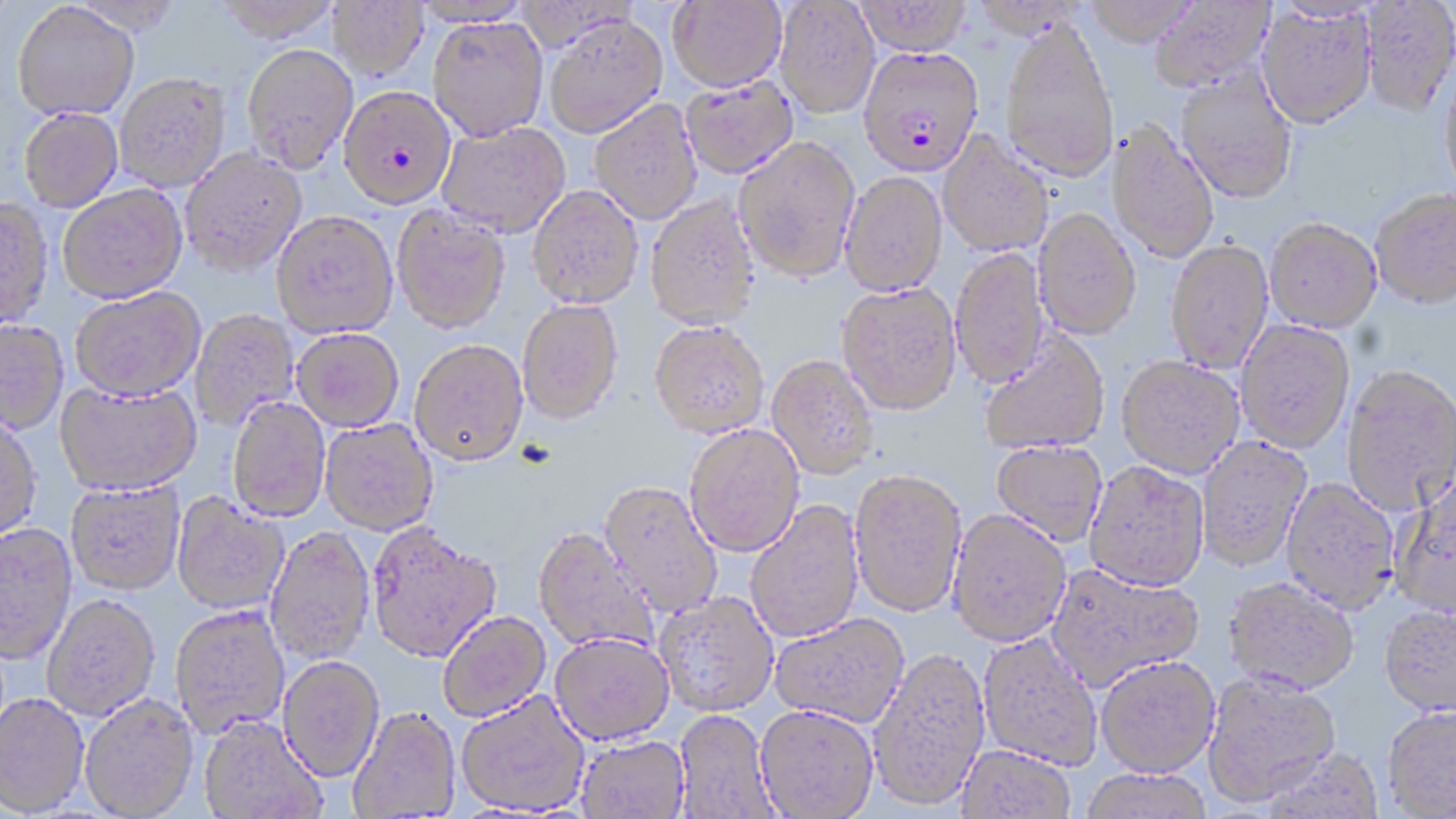

Summary:
  - Coordinate format: approximate bounding boxes as (x1,y1)-(x2,y2) corner pairs in pixels
  - Uninfected red blood cell locations: (213,0)-(343,42), (854,0)-(973,56), (1083,0)-(1201,47), (1149,0)-(1276,94), (326,1)-(429,81), (667,1)-(787,92), (775,1)-(880,119), (1360,1)-(1456,120), (12,3)-(139,123), (1257,6)-(1377,130), (543,14)-(668,139), (427,16)-(549,142), (1001,17)-(1119,183), (241,43)-(359,174), (1439,68)-(1456,202), (1174,70)-(1299,206), (115,73)-(231,192), (680,78)-(797,179), (590,99)-(702,225), (19,110)-(123,213), (438,121)-(570,239), (1105,123)-(1220,265), (937,131)-(1053,258), (734,136)-(860,283), (180,147)-(308,277), (840,172)-(948,297), (527,185)-(644,309), (58,186)-(187,305), (1370,191)-(1456,312), (645,195)-(761,330), (0,200)-(54,332), (392,205)-(511,335), (1033,209)-(1141,342), (272,212)-(398,339), (1265,221)-(1382,336), (1165,242)-(1273,375), (951,248)-(1049,390), (837,284)-(962,418), (71,288)-(205,404), (518,299)-(624,426), (191,310)-(299,431), (1236,321)-(1355,455), (0,322)-(68,435), (649,322)-(769,439), (291,329)-(404,432), (980,331)-(1110,456), (410,342)-(529,469), (767,356)-(879,480), (1116,358)-(1244,481), (1341,367)-(1456,516), (55,383)-(202,498), (227,398)-(331,523), (0,419)-(43,545), (320,420)-(437,536), (685,425)-(805,558), (1196,437)-(1311,573), (991,442)-(1107,547), (1085,463)-(1210,595), (849,473)-(966,620), (1390,477)-(1456,623), (1281,478)-(1400,617), (65,481)-(186,597), (599,483)-(723,619), (171,493)-(290,616), (746,500)-(864,644), (947,512)-(1072,650), (0,524)-(78,668), (366,524)-(501,666), (266,528)-(375,666), (533,528)-(658,655), (1045,565)-(1205,694), (1223,580)-(1358,698), (654,592)-(779,718), (42,597)-(161,722), (170,606)-(290,739), (1379,608)-(1456,719), (439,612)-(552,724), (770,616)-(910,731), (977,633)-(1103,772), (550,636)-(675,747), (869,649)-(990,814), (278,658)-(384,785), (1096,659)-(1221,781), (1202,674)-(1341,809), (456,692)-(590,817), (0,694)-(89,818), (80,695)-(200,819), (754,707)-(879,819), (1381,707)-(1456,818), (348,709)-(461,817), (673,710)-(778,819), (199,717)-(327,819), (576,737)-(690,819), (956,746)-(1077,818), (1256,749)-(1386,819), (1079,770)-(1213,819)
  - Plasmodium falciparum-infected red blood cell locations: (858,46)-(984,179), (338,85)-(457,211)
  - Slide-level diagnosis: Plasmodium falciparum
  - Stain: May-Grünwald-Giemsa
  - Magnification: 1000x
  - Image size: 1456×819 pixels
  - Field of view: single
  - Preparation: thin blood smear
  - Modality: optical microscopy